Identify the cell.
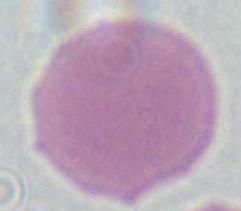

An erythrocyte.

Photomicrograph. Captured at 1000x magnification.